Name the cell type shown.
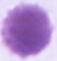
An erythrocyte.

Summary:
  - Magnification: 1000x
  - Modality: photomicrograph